Assess this cell for malaria.
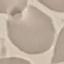

Uninfected.

{
  "stain": "Giemsa",
  "preparation": "thin smear",
  "image_type": "automatically extracted cell patch, resized to 64 × 64 pixels",
  "capture": "smartphone through the microscope eyepiece"
}